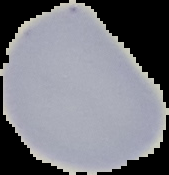

Cell region segmented out of the field of view; the surrounding area is masked to black. Image is 169×175 pixels. Result: negative for Plasmodium parasites. From a thin blood smear.